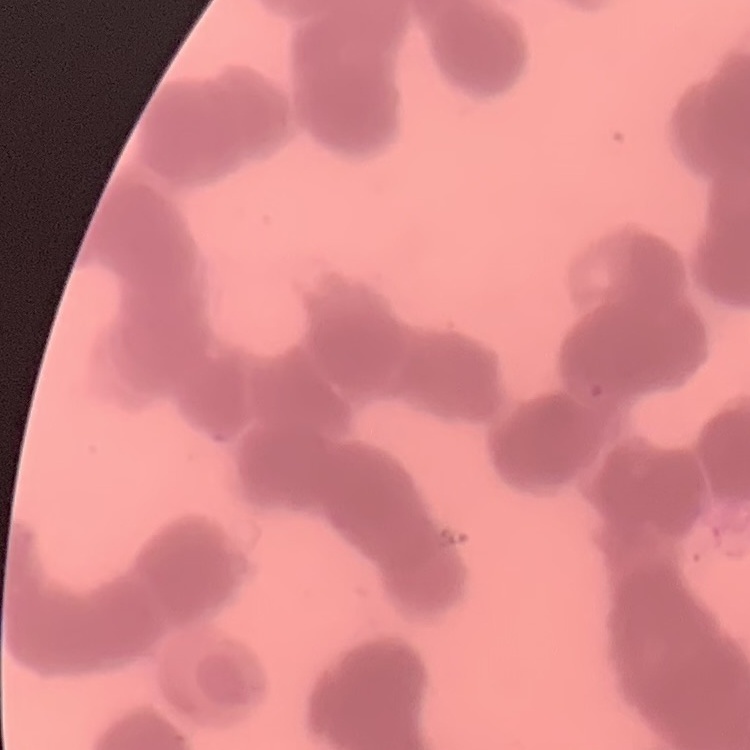

red_blood_cell_morphology: rouleaux formation
image_type: one tile cut from a larger photomicrograph
preparation: thin blood smear
stain: Field's or Giemsa